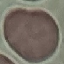

Result: negative for malaria parasites. Cell patch, automatically extracted from a larger field of view and resized to 64 × 64 pixels. Thin smear of blood. Giemsa stain. Acquired by smartphone through the microscope eyepiece.